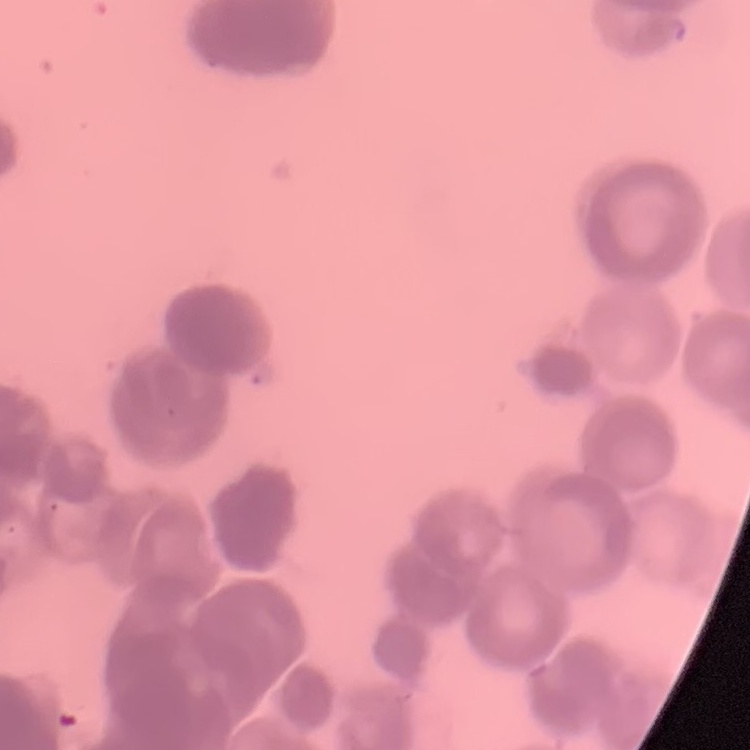

Summary:
  - Erythrocyte morphology: rouleaux formation
  - Image type: one tile cut from a larger photomicrograph
  - Preparation: thin blood film
  - Stain: Field's or Giemsa